Assess this cell for malaria.
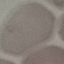

It is uninfected.

Summary:
  - Preparation: thin blood smear
  - Image type: automatically extracted cell patch, resized to 64 × 64 pixels
  - Stain: Giemsa
  - Capture: smartphone through the microscope eyepiece